Report the malaria status of this cell.
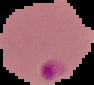

Parasitized.

image type = cell region segmented out of the field of view; surrounding area masked to black
image size = 94×85 pixels
preparation = thin blood smear